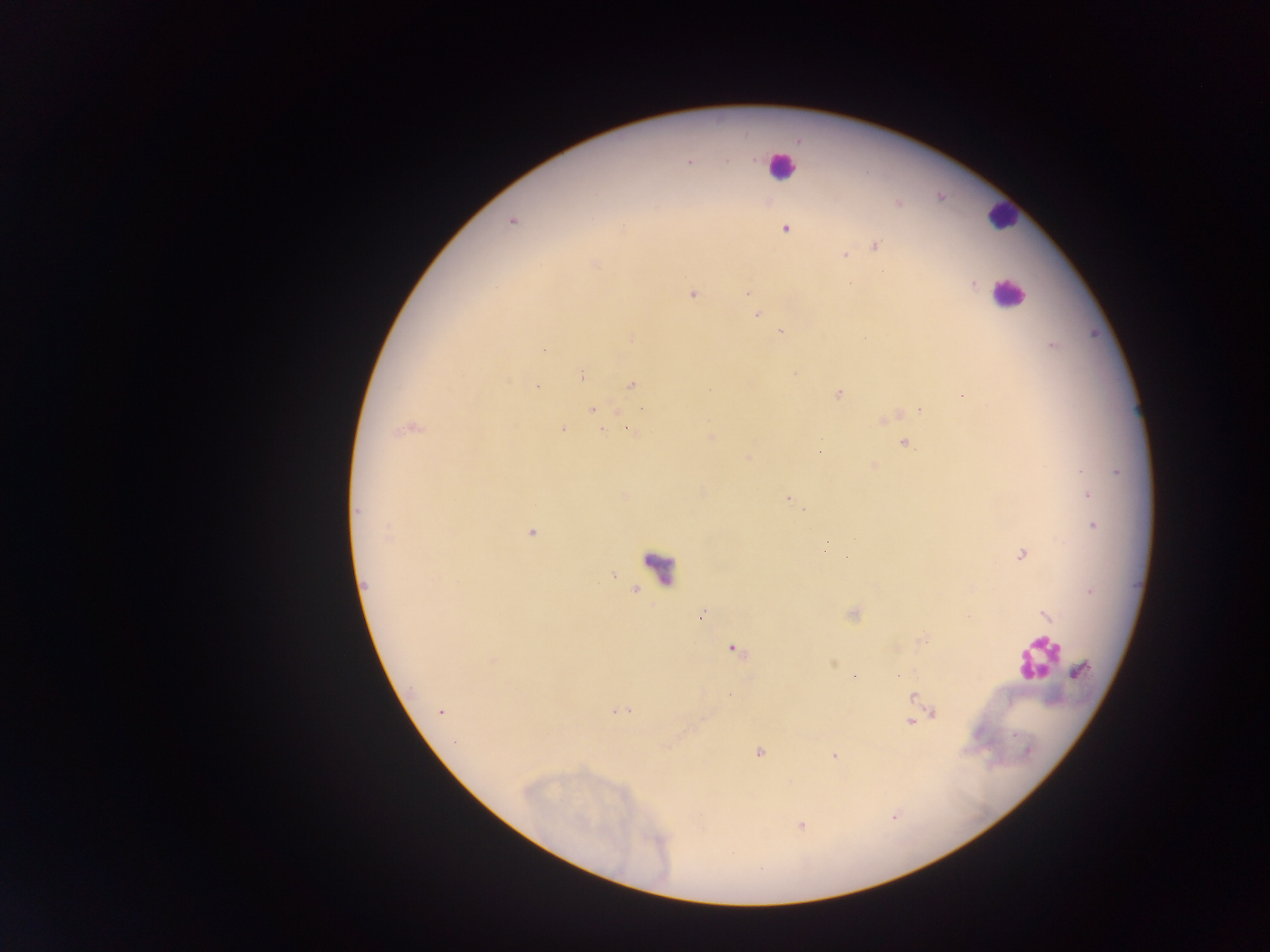
preparation: thick blood film
leukocyte_locations: 'approximate centers as (x, y) in pixels: (780, 167), (1002, 215), (1006, 295), (660, 567), (1037, 658)'
country: Ghana
plasmodium_parasite_locations: 'approximate centers as (x, y) in pixels: (689, 162), (512, 222), (786, 230), (876, 246), (843, 255), (595, 264), (973, 284), (747, 294), (693, 295), (757, 315), (780, 331), (632, 337), (1053, 346), (543, 350), (795, 373), (582, 376), (632, 385), (538, 387), (838, 394), (963, 396), (593, 409), (919, 410), (642, 411), (884, 420), (407, 429), (563, 429), (628, 429), (602, 430), (711, 436), (904, 443), (819, 451), (874, 467), (1080, 471), (1088, 494), (787, 499), (805, 509), (358, 510), (1093, 525), (531, 532), (388, 537), (827, 543), (1022, 555), (1045, 614), (702, 615), (735, 651), (492, 660), (1081, 670), (915, 697), (619, 711), (440, 712), (935, 714), (910, 722), (1015, 735), (759, 752), (834, 755), (801, 825)'
capture: mobile-phone photograph through a microscope
field_of_view: single
image_size: 1270×952 pixels